Identify the parasite.
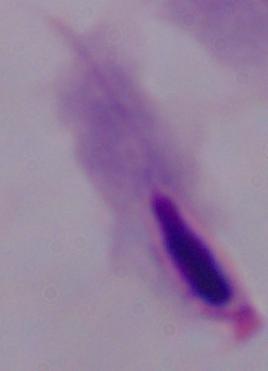

This is a trichomonad.

Summary:
  - Magnification: 1000x
  - Modality: micrograph